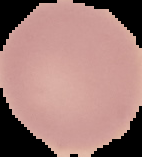

Image is 142×157 pixels. The area outside the segmented cell region is set to black. From a thin blood film. Malaria status: uninfected.